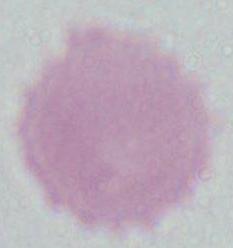

Summary:
  - Identification: red blood cell
  - Modality: photomicrograph
  - Magnification: 1000x